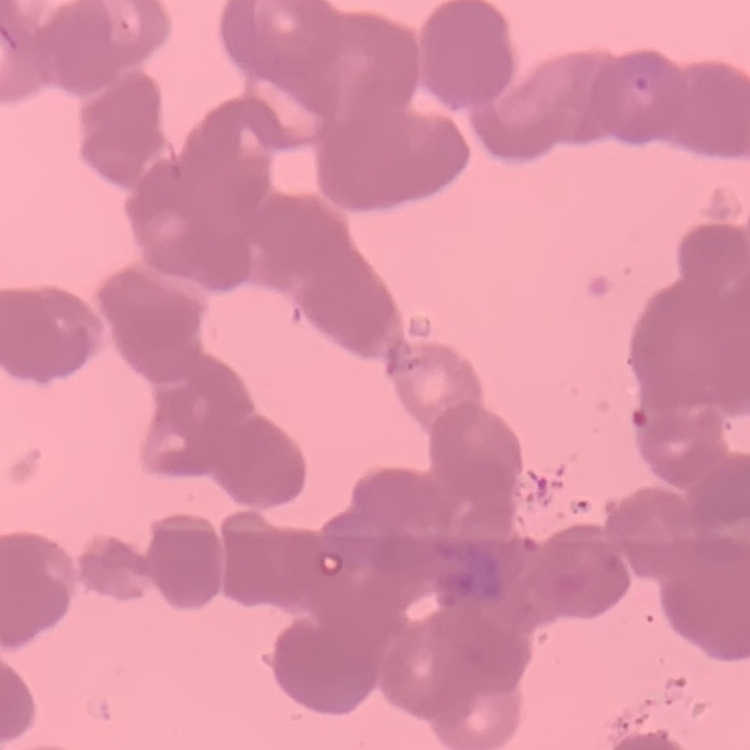
red_blood_cell_morphology: rouleaux formation
preparation: thin peripheral smear
image_type: square crop of a larger photomicrograph
stain: Field's or Giemsa